Assess the morphology of the red blood cells.
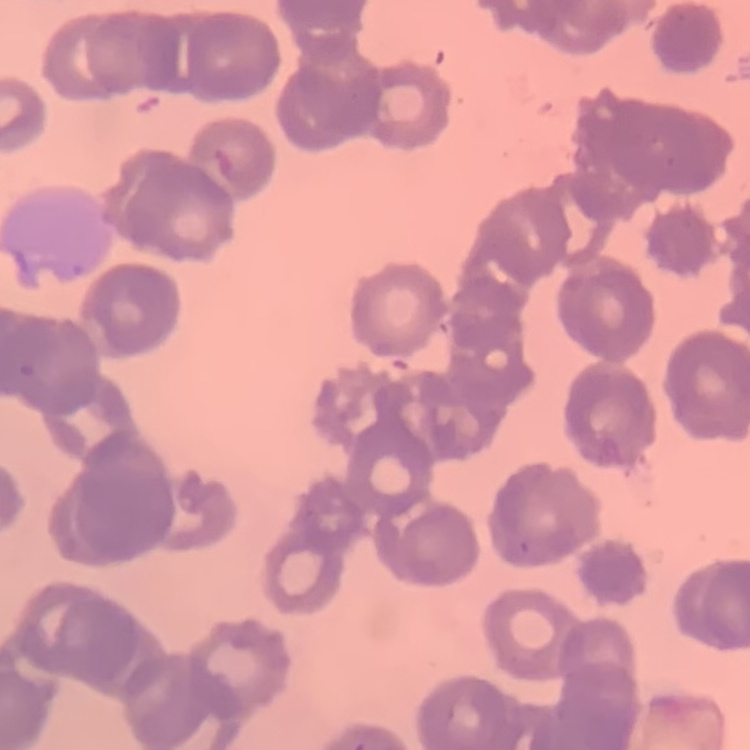

Rouleaux formation.

{
  "image_type": "square crop of a larger photomicrograph",
  "preparation": "thin blood film",
  "stain": "Field's or Giemsa"
}